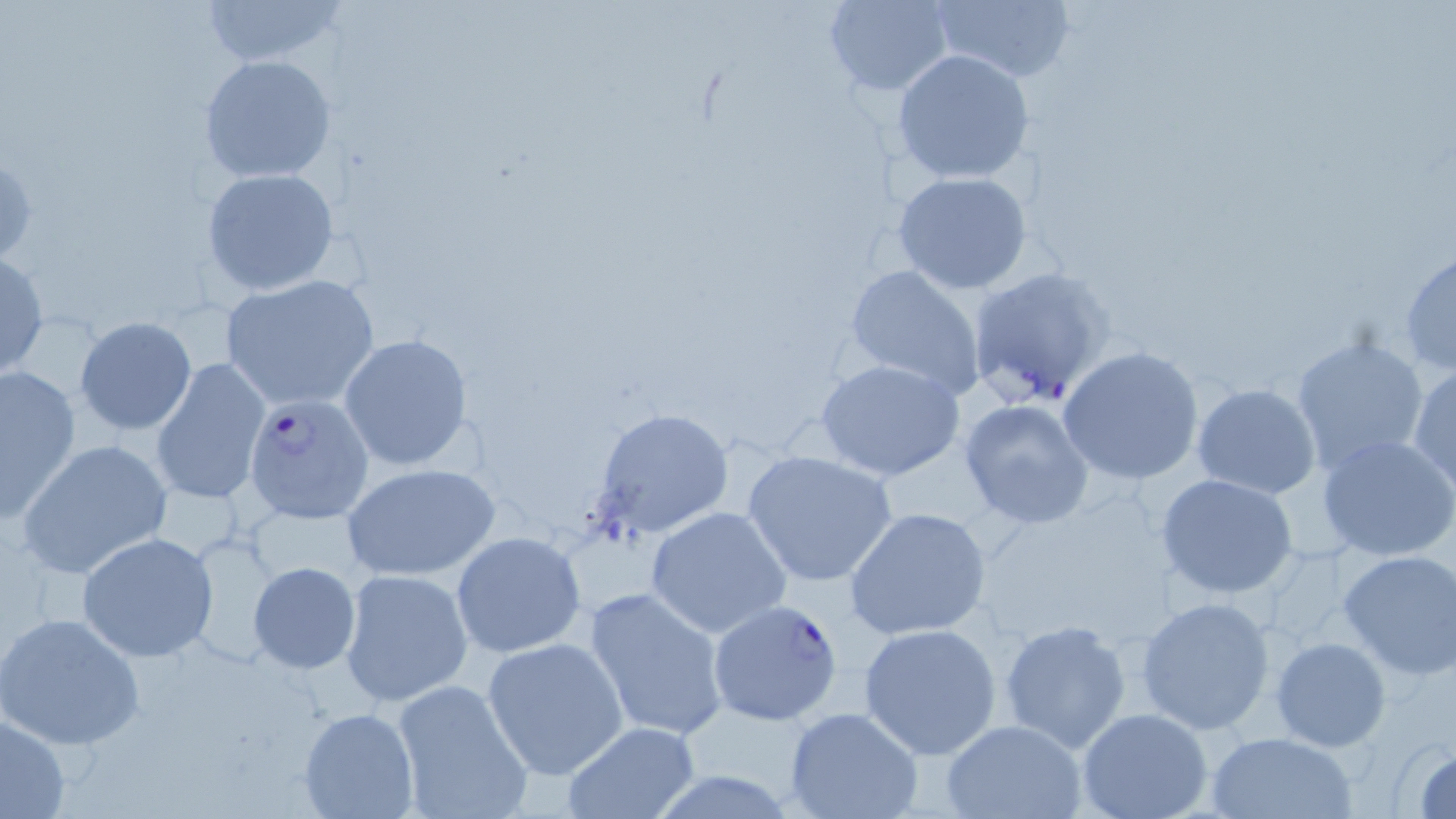

slide-level diagnosis = Plasmodium falciparum
preparation = thin blood smear
uninfected red blood cell locations = approximate bounding boxes as (x1,y1)-(x2,y2) corner pairs in pixels: (200,0)-(345,70), (822,0)-(955,94), (926,1)-(1077,84), (892,49)-(1034,184), (199,54)-(336,183), (204,167)-(340,295), (892,170)-(1033,294), (1400,246)-(1455,377), (0,253)-(47,377), (843,264)-(988,401), (220,274)-(380,413), (75,317)-(196,435), (336,333)-(476,472), (1290,336)-(1429,473), (1059,346)-(1205,486), (149,358)-(269,506), (817,359)-(966,482), (1408,363)-(1456,494), (0,364)-(81,522), (1191,384)-(1321,499), (958,398)-(1095,529), (591,407)-(734,539), (1316,434)-(1456,563), (19,439)-(173,581), (741,449)-(900,588), (340,462)-(502,581), (1156,473)-(1297,600), (644,507)-(791,639), (843,507)-(993,641), (449,531)-(587,659), (75,532)-(221,663), (182,533)-(284,668), (1337,550)-(1456,682), (248,562)-(360,674), (339,567)-(474,708), (585,587)-(728,740), (1134,596)-(1276,734), (1,612)-(146,749), (999,619)-(1133,754), (859,622)-(1005,760), (482,636)-(629,779), (1270,636)-(1392,752), (390,677)-(533,819), (297,708)-(419,819), (785,708)-(923,819), (1078,709)-(1213,819), (0,713)-(71,818), (939,718)-(1087,819), (559,720)-(701,819), (1206,729)-(1357,818), (1403,740)-(1456,818)
stain = May-Grünwald-Giemsa
image size = 1456×819 pixels
modality = light microscopy
Plasmodium falciparum-infected red blood cell locations = approximate bounding boxes as (x1,y1)-(x2,y2) corner pairs in pixels: (965,268)-(1114,410), (244,393)-(375,523), (708,599)-(844,727)
field of view = one of a larger specimen
magnification = 1000x